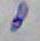
Summary:
  - Identification: Toxoplasma gondii
  - Magnification: 1000x
  - Modality: micrograph